Classify this cell by malaria status.
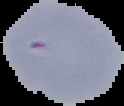

Uninfected.

Summary:
  - Preparation: thin blood smear
  - Image size: 124×106 pixels
  - Image type: cell region segmented out of the field of view; surrounding area masked to black